Locate every leukocyte (white blood cell).
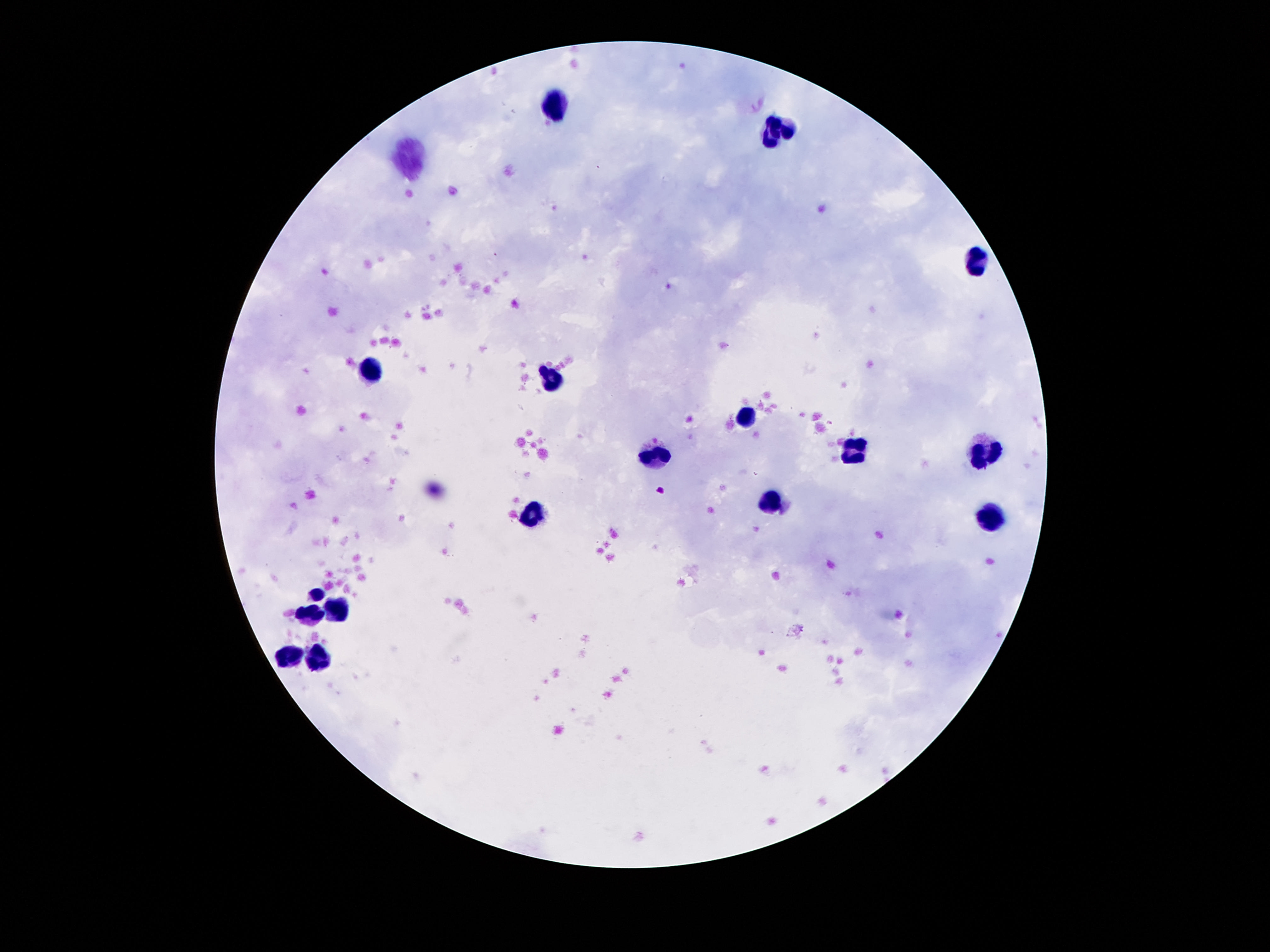
Approximate object centers, in pixels from the top-left corner.
Leukocytes: (x=554, y=109), (x=775, y=131), (x=974, y=261), (x=369, y=365), (x=554, y=379), (x=749, y=418), (x=853, y=449), (x=981, y=454), (x=652, y=458), (x=769, y=502), (x=532, y=515), (x=990, y=517), (x=316, y=595), (x=335, y=608), (x=313, y=615), (x=288, y=657), (x=319, y=657).

capture = smartphone camera through the microscope eyepiece
patient malaria status = not infected
field of view = one from this slide
preparation = thick peripheral-blood smear
image size = 1270×952 pixels
magnification = 100x
stain = Giemsa